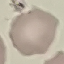
Result: no malaria parasites detected. Photographed with a smartphone camera at the microscope eyepiece. Cell patch, automatically extracted from a larger field of view and resized to 64 × 64 pixels. Thin blood film. Giemsa stain.